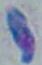

magnification = 1000x
identification = Toxoplasma gondii
modality = micrograph